Report the malaria status.
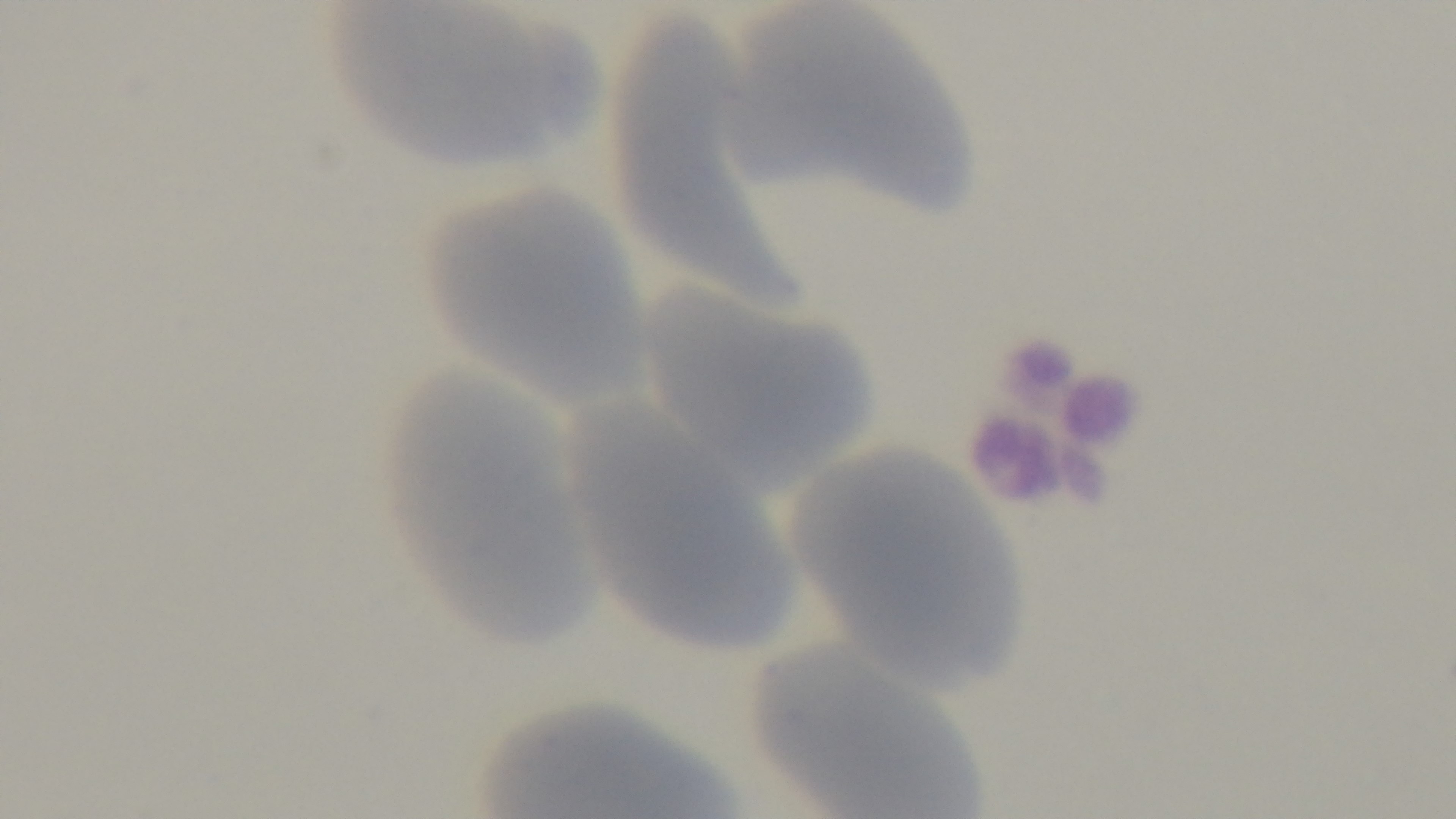
Uninfected.

One field from the slide. Photomicrograph. Preparation: thin smear. Giemsa-stained. Mounted 4K digital camera. 100x oil-immersion objective.